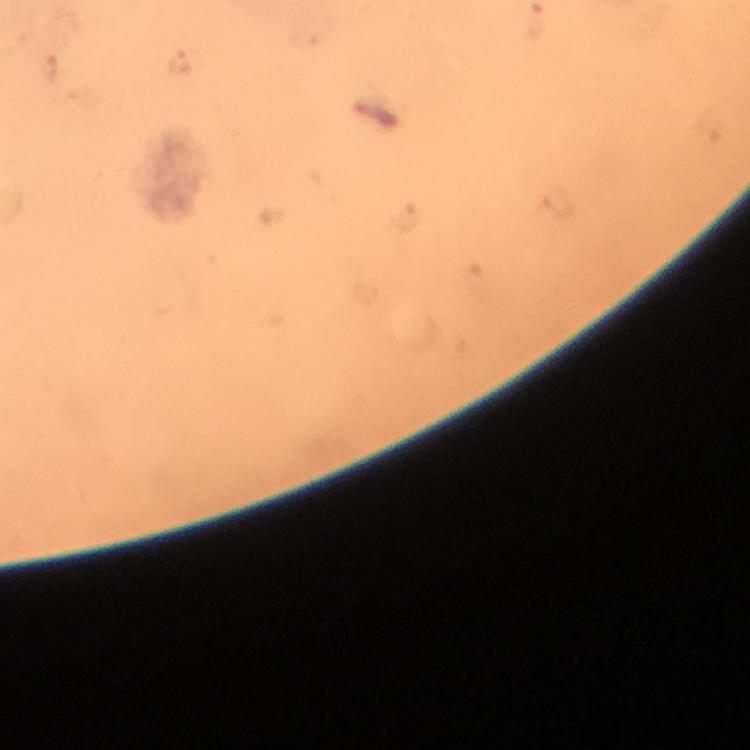
Approximate centers as [x, y] in pixels.
Summary:
  - Malaria parasite locations: [178, 62]
  - Magnification: 100x
  - Cropped from: one field of view
  - Preparation: thick blood smear
  - Immersion oil: applied
  - Context: from a diagnostic examination for malaria
  - Image size: 750×750 pixels
  - Capture: smartphone camera through the microscope
  - Stain: Giemsa